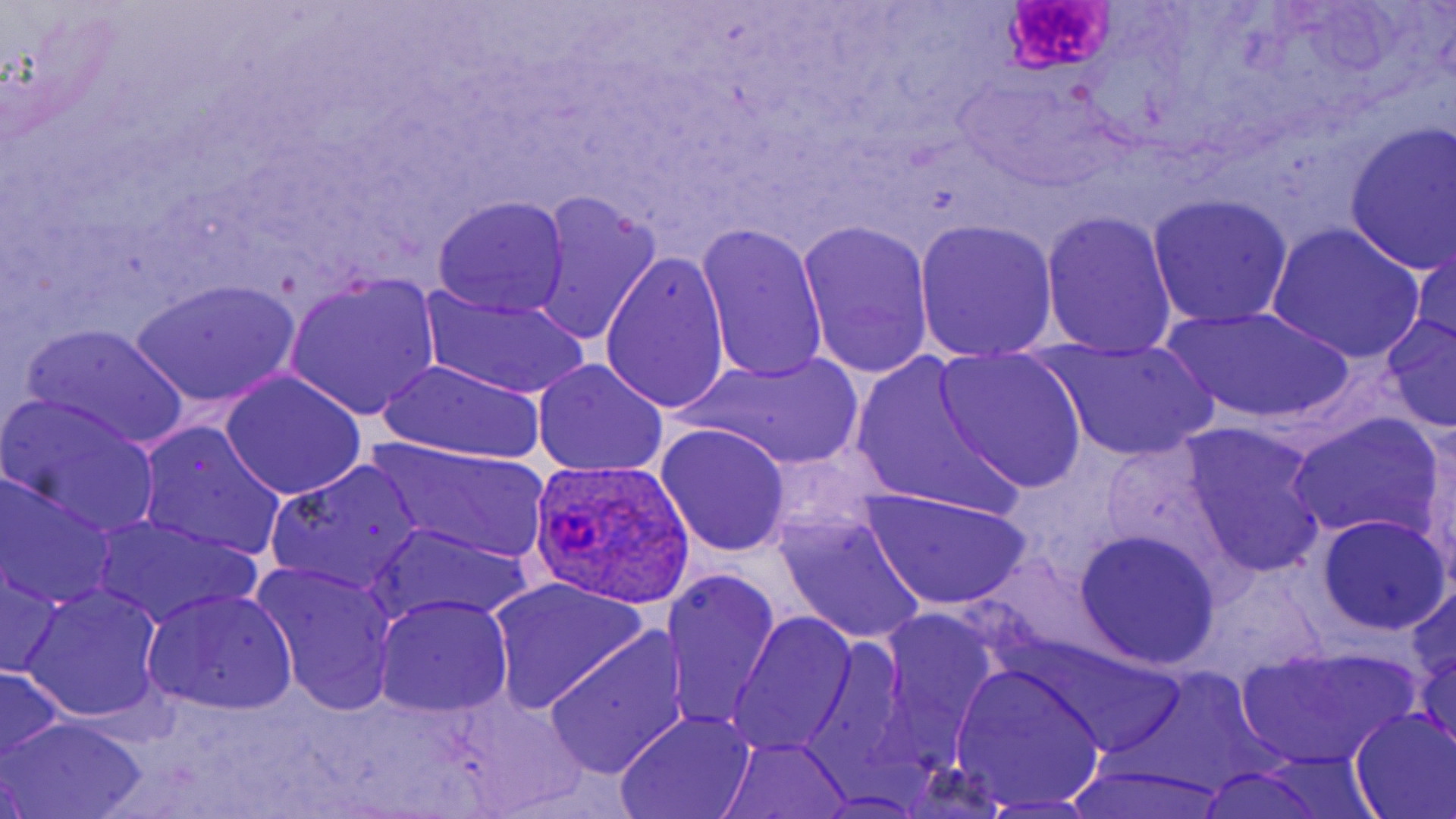

plasmodium_ovale_infected_red_blood_cell_locations: 'approximate bounding boxes as (x1, y1, x2, y2) in pixels: (528, 456, 691, 604)'
slide_level_diagnosis: Plasmodium ovale
modality: optical microscopy
magnification: 1000x
field_of_view: one of a larger specimen
image_size: 1456×819 pixels
stain: May-Grünwald-Giemsa
uninfected_red_blood_cell_locations: 'approximate bounding boxes as (x1, y1, x2, y2) in pixels: (1342, 121, 1455, 276), (527, 190, 662, 346), (1145, 194, 1294, 329), (431, 195, 570, 319), (1040, 209, 1178, 358), (912, 217, 1059, 363), (796, 218, 935, 379), (695, 221, 829, 385), (1266, 221, 1430, 365), (1408, 232, 1456, 365), (599, 248, 731, 417), (281, 272, 444, 420), (128, 275, 301, 409), (417, 285, 591, 401), (1162, 305, 1354, 426), (1379, 313, 1456, 439), (19, 323, 191, 451), (1032, 338, 1223, 462), (933, 346, 1087, 492), (680, 349, 865, 471), (847, 352, 1019, 519), (377, 356, 545, 466), (532, 358, 669, 478), (220, 369, 366, 502), (2, 392, 160, 537), (1285, 413, 1447, 544), (135, 420, 287, 562), (1179, 421, 1330, 580), (655, 422, 791, 556), (1416, 425, 1456, 593), (1098, 434, 1237, 571), (369, 435, 551, 568), (264, 458, 424, 597), (0, 472, 116, 610), (858, 484, 1032, 610), (774, 510, 926, 643), (87, 512, 262, 631), (1316, 513, 1451, 635), (368, 521, 538, 626), (1074, 530, 1220, 670), (2, 553, 63, 681), (249, 560, 401, 713), (659, 566, 780, 733), (1407, 570, 1456, 684), (487, 575, 649, 713), (19, 583, 164, 723), (141, 587, 297, 714), (374, 594, 513, 716), (728, 611, 855, 754), (1413, 622, 1456, 762), (544, 628, 691, 780), (1235, 643, 1415, 770), (951, 662, 1106, 811), (1, 665, 71, 768), (1349, 708, 1456, 819), (613, 711, 753, 819), (1, 714, 150, 819), (722, 736, 851, 817), (1064, 762, 1232, 819), (1191, 767, 1329, 819)'
preparation: thin blood smear